Draw a bounding box around every leukocyte (white blood cell).
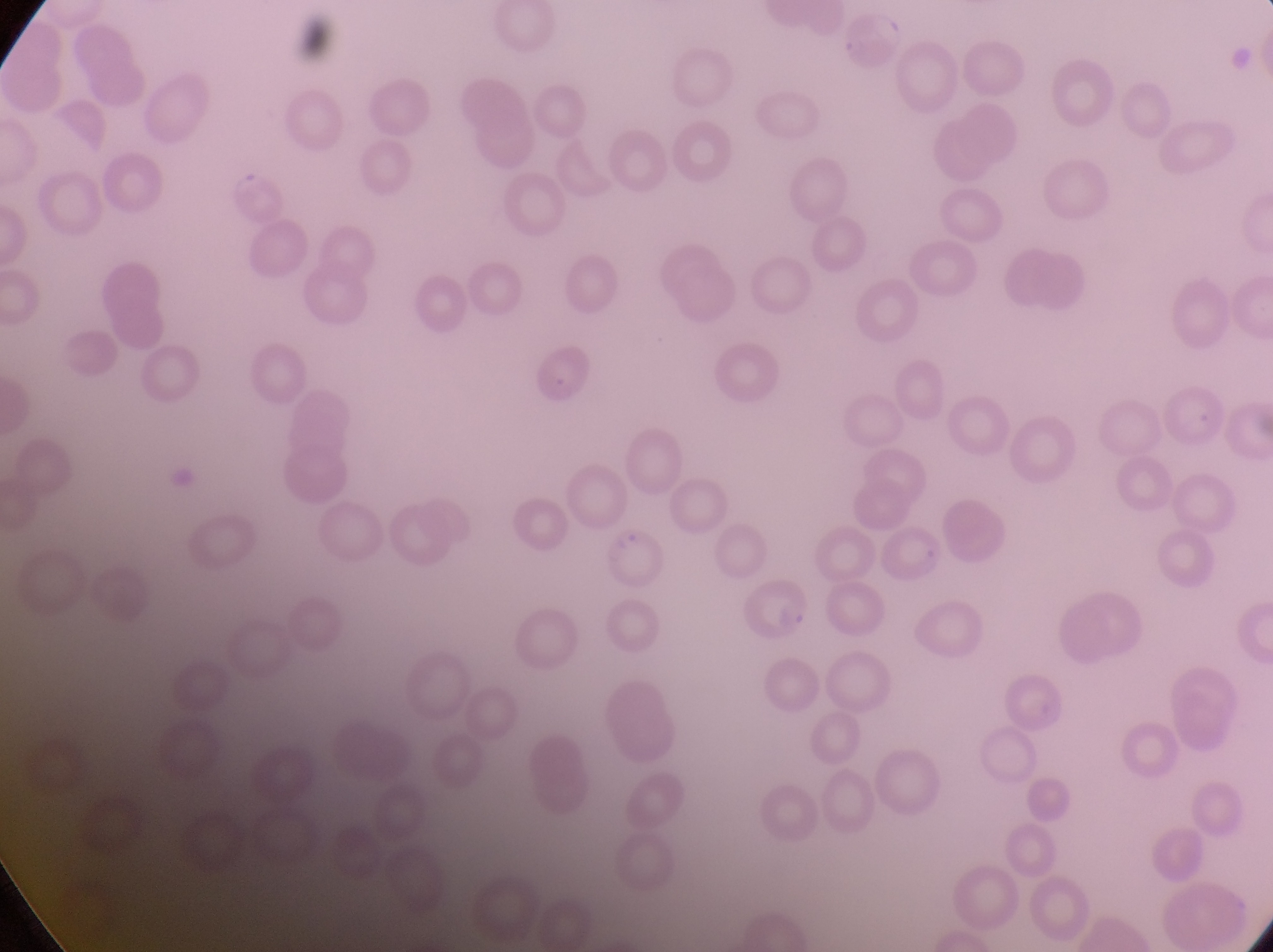

No leukocytes observed.

image size = 1273×952 pixels
field of view = single
parasitised red blood cell locations = approximate bounding boxes as (left, top, right, bottom) in pixels: (524, 339, 593, 409), (606, 529, 673, 594), (739, 586, 819, 646)
country = Uganda
capture = smartphone photograph through the eyepiece of an Olympus CX-23 microscope
magnification = 1000x
preparation = thin blood smear